Assess this cell for malaria.
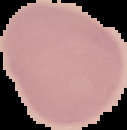

It is uninfected.

From a thin blood smear. Segmented cell region on a black background. Image is 127×130 pixels.